Assess this cell for malaria.
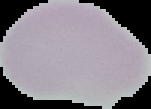

Uninfected.

Summary:
  - Image size: 151×109 pixels
  - Image type: segmented cell region on a black background
  - Preparation: thin blood film